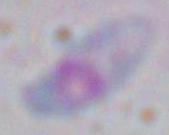
Micrograph. Toxoplasma gondii is seen. 1000x magnification.